Identify the parasite.
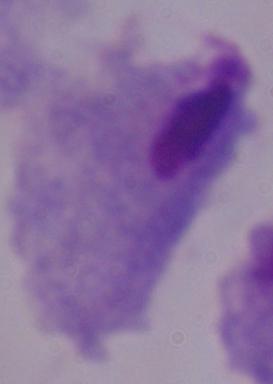
This is a trichomonad.

1000x magnification. Micrograph.